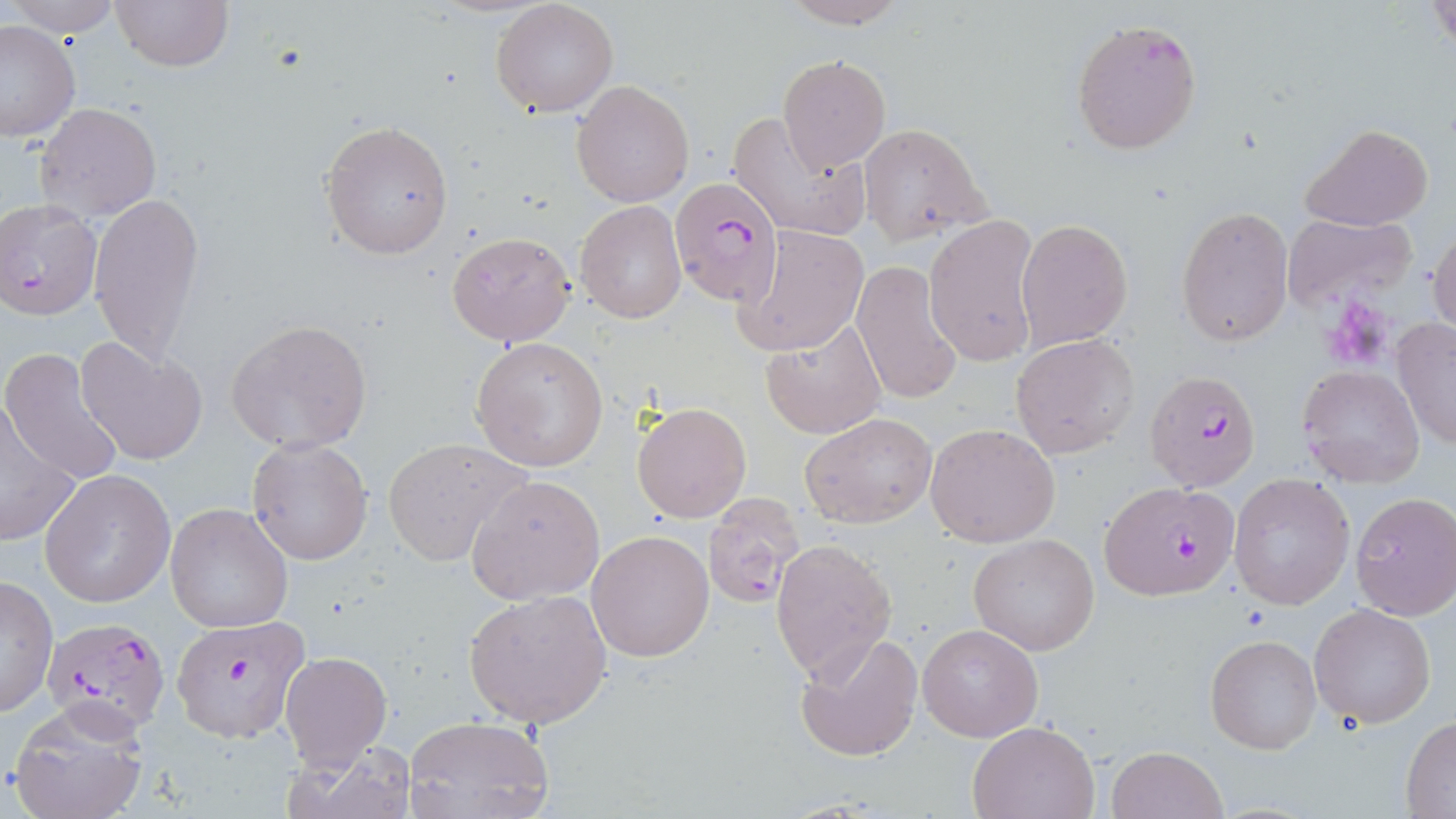
Summary:
  - Coordinate format: approximate bounding boxes as (x1,y1)-(x2,y2) corner pairs in pixels
  - Plasmodium falciparum-infected red blood cell locations: (670,175)-(786,308), (0,201)-(102,320), (1145,368)-(1263,493), (1099,482)-(1241,602), (701,493)-(807,611), (172,615)-(309,741), (41,618)-(171,734)
  - Uninfected red blood cell locations: (8,0)-(124,36), (113,0)-(232,72), (779,0)-(910,28), (1429,0)-(1454,55), (490,1)-(619,116), (1070,16)-(1202,155), (0,18)-(80,141), (776,55)-(892,175), (571,80)-(694,208), (34,101)-(163,222), (728,111)-(874,242), (319,120)-(454,259), (857,122)-(991,245), (1301,123)-(1433,231), (88,191)-(204,362), (574,201)-(686,322), (1175,203)-(1292,347), (1281,212)-(1419,313), (924,215)-(1042,368), (1015,219)-(1133,351), (1430,220)-(1456,341), (731,225)-(869,357), (447,229)-(575,347), (852,259)-(967,406), (1392,316)-(1456,450), (760,317)-(887,440), (226,319)-(374,452), (1012,334)-(1141,459), (471,335)-(609,472), (76,336)-(208,466), (2,350)-(126,486), (1298,365)-(1425,486), (631,401)-(753,523), (1,404)-(80,543), (800,411)-(936,529), (923,422)-(1062,549), (246,437)-(373,566), (383,438)-(529,567), (40,469)-(176,607), (1228,474)-(1355,612), (466,476)-(605,604), (1349,492)-(1456,620), (164,503)-(293,633), (585,529)-(715,663), (968,533)-(1099,655), (770,539)-(897,682), (0,574)-(57,719), (462,588)-(613,729), (1309,603)-(1437,728), (917,623)-(1043,742), (793,631)-(922,764), (1205,634)-(1322,756), (279,649)-(392,773), (9,701)-(152,819), (402,715)-(553,819), (1402,718)-(1456,816), (966,720)-(1099,819), (285,741)-(416,818), (1105,746)-(1228,819)
  - Platelet locations: (1319,298)-(1396,366)
  - Slide-level diagnosis: Plasmodium falciparum
  - Magnification: 1000x
  - Image size: 1456×819 pixels
  - Modality: light microscopy
  - Preparation: thin blood film
  - Field of view: single
  - Stain: May-Grünwald-Giemsa